Describe the morphology of the red blood cells.
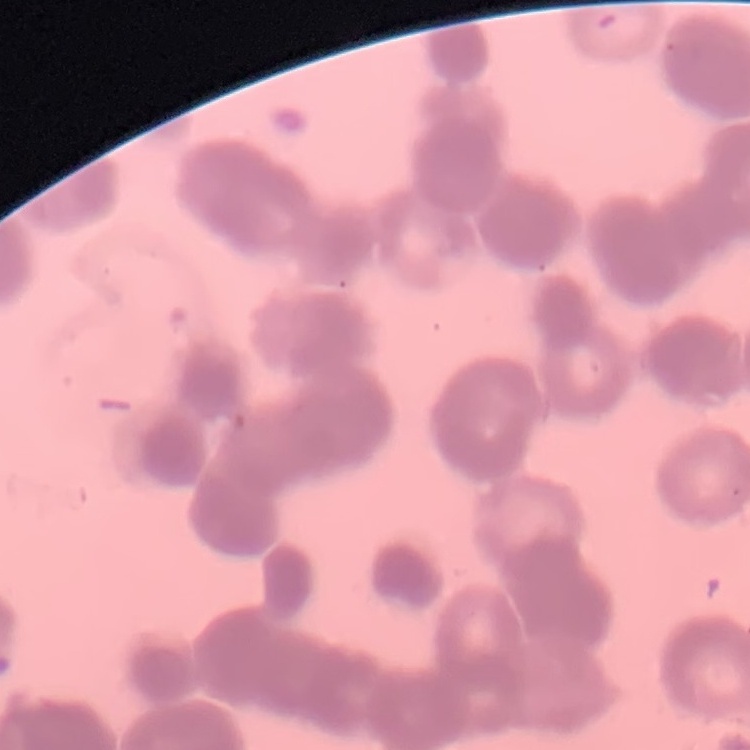

They show rouleaux formation.

Summary:
  - Image type: one tile cut from a larger photomicrograph
  - Stain: Field's or Giemsa
  - Preparation: thin blood film